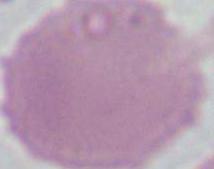

{
  "magnification": "1000x",
  "modality": "photomicrograph",
  "identification": "red blood cell"
}